Report the malaria status of this cell.
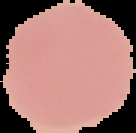
Uninfected.

image size = 136×133 pixels
image type = segmented cell region on a black background
preparation = thin blood smear